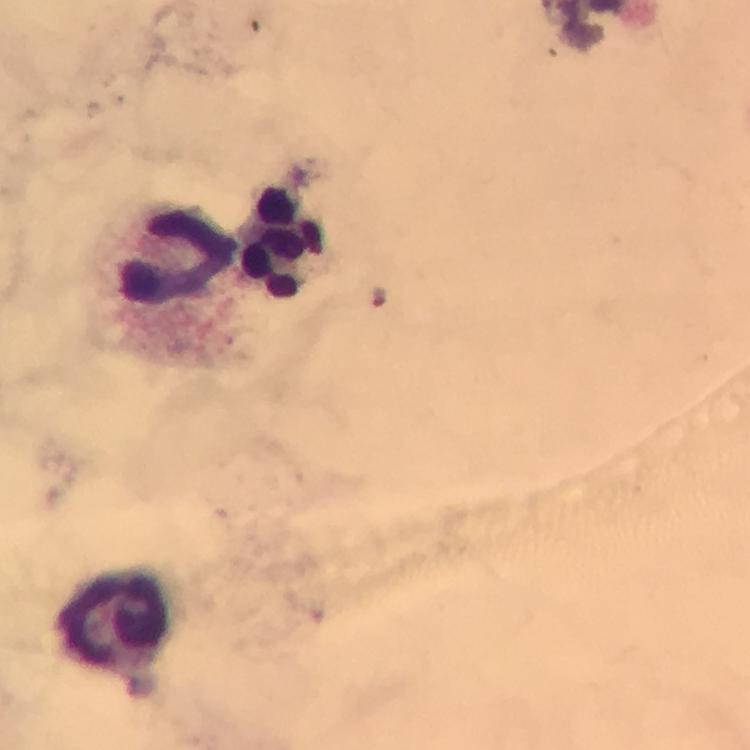

{
  "cropped_from": "a single field of view",
  "plasmodium_parasites": "none detected",
  "stain": "Giemsa",
  "preparation": "thick smear",
  "image_size": "750×750 pixels",
  "leukocyte_locations": "approximate centers as [x, y] in pixels: [284, 243], [179, 257], [117, 626]",
  "immersion_oil": "applied",
  "capture": "smartphone photograph through a microscope",
  "magnification": "100x",
  "context": "from a diagnostic examination for malaria"
}